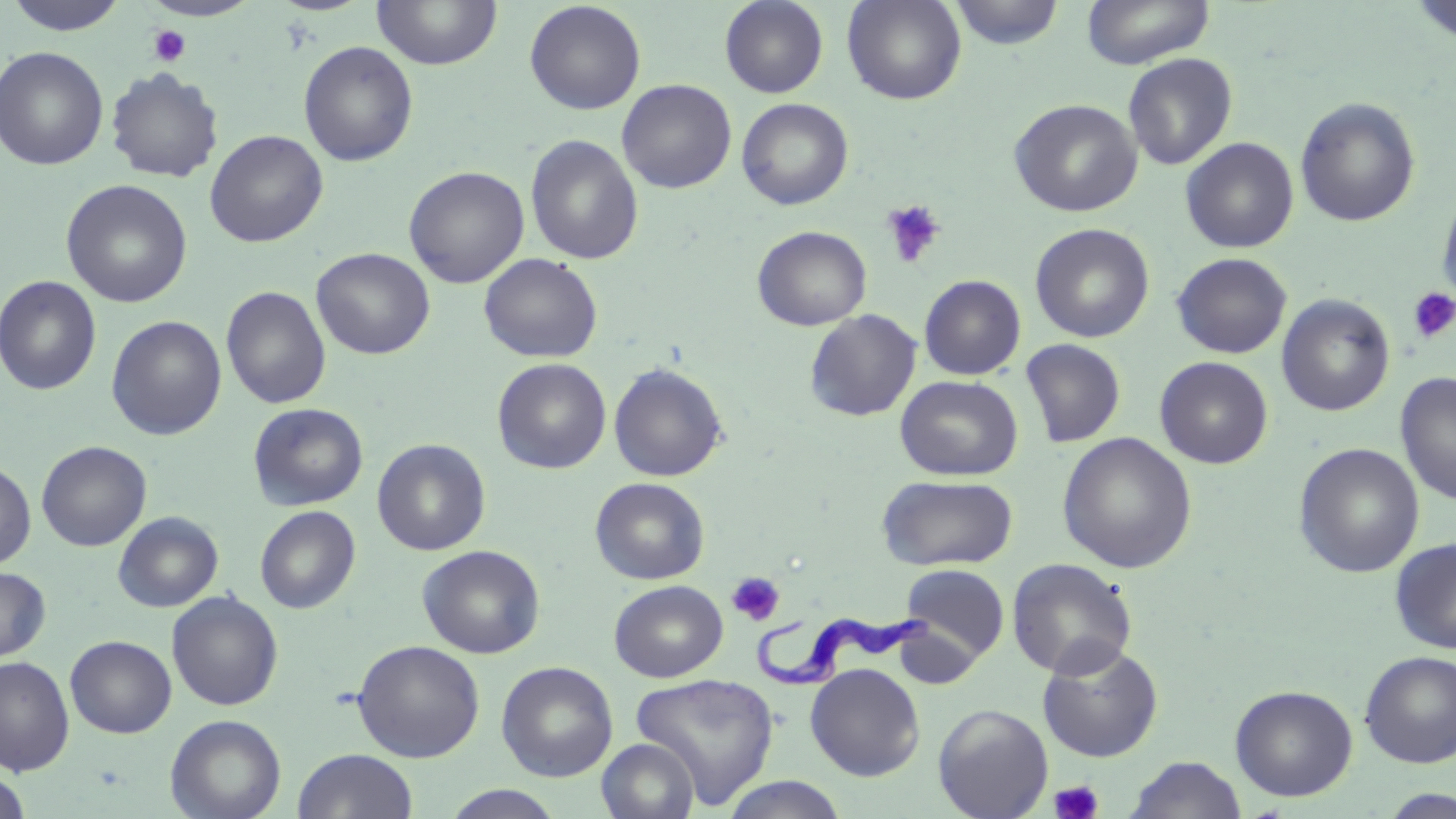
{
  "slide_level_diagnosis": "Trypanosoma brucei",
  "stain": "May-Grünwald-Giemsa",
  "trypanosoma_brucei_locations": "approximate bounding boxes as (x1,y1)-(x2,y2) corner pairs in pixels: (745,609)-(937,695)",
  "platelet_locations": "approximate bounding boxes as (x1,y1)-(x2,y2) corner pairs in pixels: (148,24)-(191,67), (881,200)-(946,269), (1408,288)-(1456,343), (727,571)-(785,626), (1049,780)-(1104,819)",
  "modality": "light microscopy",
  "preparation": "thin blood film",
  "image_size": "1456×819 pixels",
  "magnification": "1000x",
  "uninfected_red_blood_cell_locations": "approximate bounding boxes as (x1,y1)-(x2,y2) corner pairs in pixels: (142,0)-(262,22), (371,0)-(503,70), (720,0)-(828,98), (842,0)-(967,105), (949,0)-(1065,50), (1082,0)-(1215,69), (4,1)-(133,35), (524,1)-(646,115), (1410,2)-(1456,43), (298,41)-(418,166), (1,46)-(108,170), (1123,53)-(1237,170), (106,67)-(224,183), (617,79)-(737,194), (1295,96)-(1420,227), (737,98)-(853,210), (1009,98)-(1142,217), (205,129)-(328,248), (525,134)-(644,265), (1181,137)-(1299,253), (404,165)-(529,288), (61,179)-(193,308), (1437,188)-(1456,311), (1029,223)-(1155,343), (752,226)-(872,331), (311,247)-(435,359), (1172,252)-(1291,359), (479,253)-(603,363), (1,275)-(102,396), (919,275)-(1026,380), (221,286)-(331,409), (1277,294)-(1395,416), (804,309)-(922,422), (106,315)-(227,441), (1020,338)-(1126,448), (1155,356)-(1273,469), (492,357)-(611,473), (608,362)-(728,482), (1395,372)-(1456,506), (895,375)-(1023,481), (248,402)-(368,511), (1057,433)-(1198,574), (372,439)-(490,556), (36,441)-(152,552), (1293,443)-(1424,578), (0,460)-(36,569), (876,474)-(1018,571), (590,477)-(709,585), (255,506)-(360,614), (113,511)-(223,612), (1390,538)-(1456,654), (417,544)-(545,659), (1006,557)-(1137,679), (899,563)-(1011,666), (0,566)-(51,662), (609,580)-(728,682), (166,590)-(283,711), (65,635)-(176,738), (352,640)-(485,762), (1037,641)-(1163,762), (1359,650)-(1456,768), (1,656)-(74,775), (496,661)-(618,781), (805,663)-(925,781), (630,672)-(780,808), (1230,684)-(1358,801), (933,703)-(1053,819), (165,714)-(286,819), (597,738)-(700,819), (292,749)-(418,819), (1124,755)-(1248,818), (0,771)-(32,818), (719,775)-(850,818), (441,784)-(567,819), (1380,788)-(1456,818)",
  "field_of_view": "single"
}